Comment on the morphology of the red blood cells.
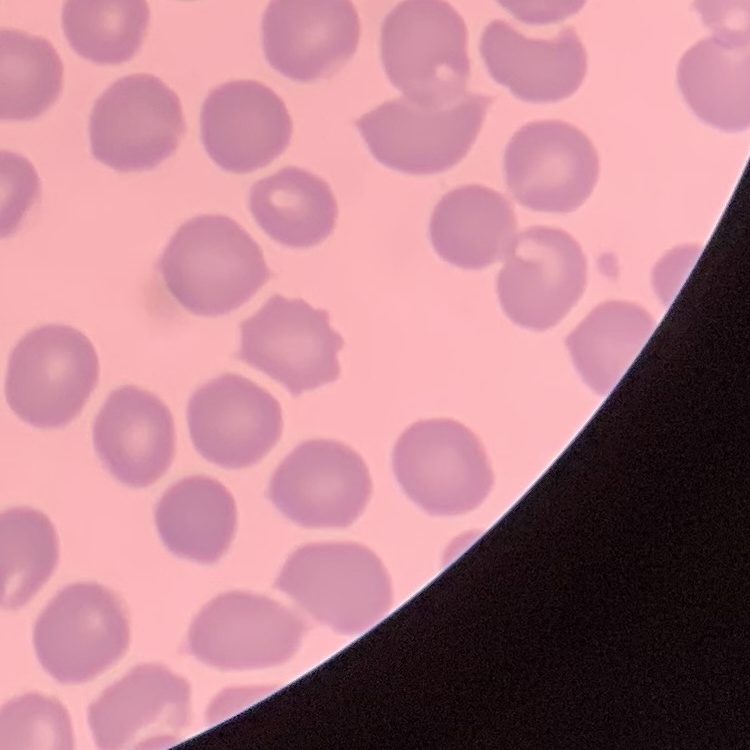

They show no rouleaux formation.

image type = one tile cut from a larger photomicrograph
preparation = thin blood film
stain = Field's or Giemsa